Outline each Plasmodium falciparum-infected red blood cell.
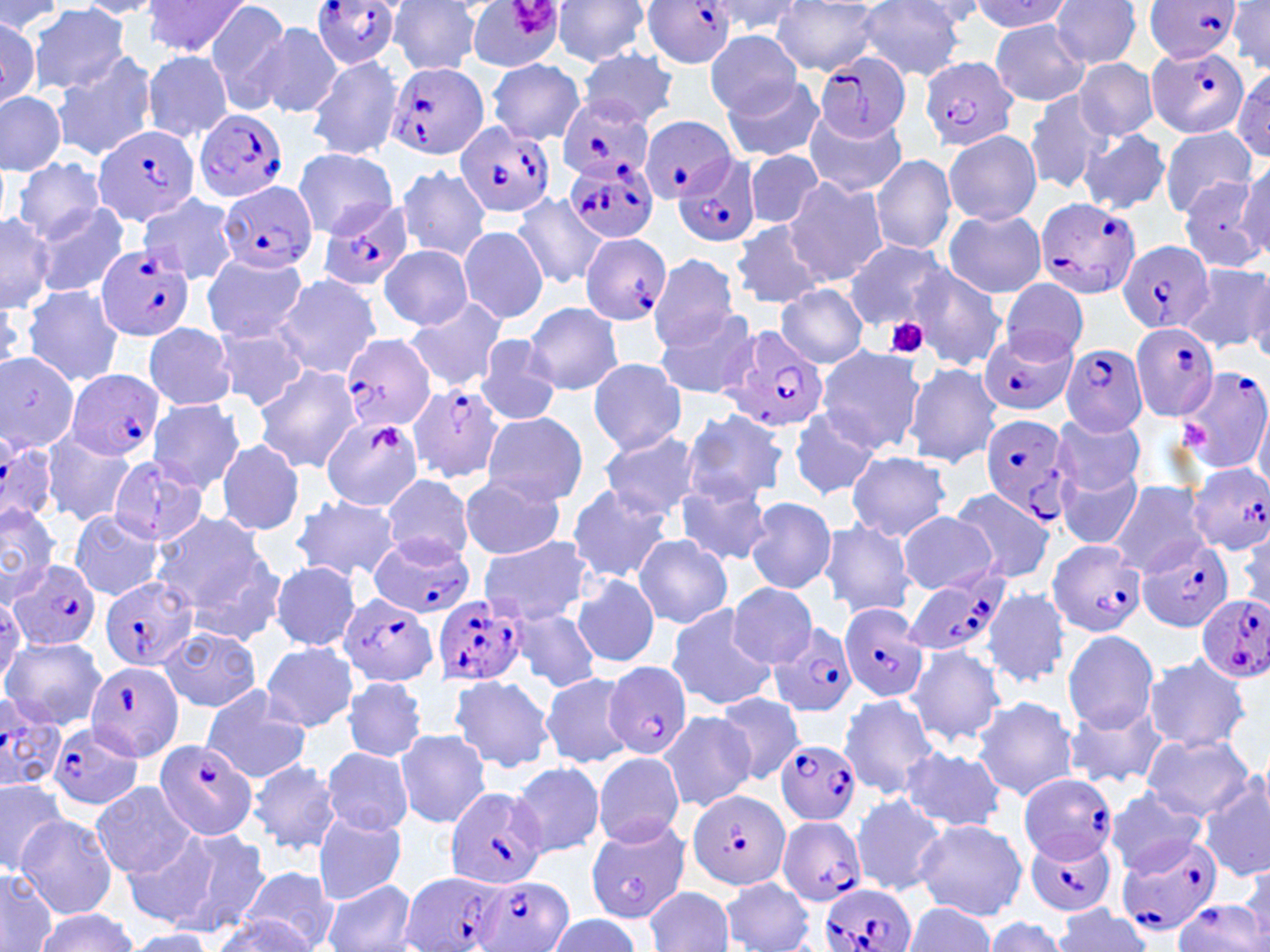
Approximate bounding boxes as [x1, y1, x2, y2] in pixels.
Plasmodium falciparum-infected red blood cells (subset): [309, 0, 402, 67], [641, 0, 737, 69], [1146, 1, 1240, 60], [1148, 42, 1250, 139], [816, 50, 912, 144], [920, 56, 1020, 151], [384, 62, 489, 161], [558, 96, 657, 183], [196, 108, 290, 204], [641, 117, 736, 202], [454, 121, 557, 219], [92, 123, 201, 226], [672, 155, 760, 245], [565, 156, 658, 245], [216, 181, 316, 275], [317, 197, 415, 292], [1032, 197, 1143, 302], [578, 233, 672, 326], [1118, 242, 1213, 334], [97, 243, 197, 342], [1130, 321, 1221, 423], [720, 326, 830, 432], [979, 327, 1077, 417], [340, 334, 436, 434], [1060, 343, 1149, 437], [1178, 367, 1270, 477], [68, 370, 164, 462], [401, 379, 508, 480], [978, 413, 1077, 526], [0, 441, 60, 525], [1185, 463, 1270, 555], [368, 533, 475, 619], [1135, 535, 1233, 631], [1045, 537, 1145, 637], [8, 558, 103, 653], [101, 575, 199, 673], [339, 592, 440, 689], [432, 595, 531, 685], [1196, 595, 1270, 682], [837, 603, 929, 704], [768, 621, 860, 719], [602, 660, 691, 762], [86, 662, 185, 761], [0, 696, 63, 794], [44, 721, 143, 812], [152, 738, 259, 840], [774, 739, 863, 827], [1018, 773, 1117, 865], [444, 786, 550, 888], [687, 790, 792, 891], [777, 816, 868, 907], [1025, 829, 1116, 918], [1115, 834, 1222, 936], [401, 871, 510, 952], [475, 875, 571, 952], [817, 884, 915, 952], [1173, 898, 1265, 952].

Summary:
  - Uninfected red blood cell locations (subset): [142, 0, 251, 59], [464, 0, 566, 71], [551, 0, 653, 67], [706, 0, 801, 37], [970, 0, 1073, 31], [1229, 0, 1270, 77], [72, 1, 165, 18], [204, 1, 290, 109], [389, 1, 487, 76], [772, 1, 882, 74], [856, 1, 967, 79], [1049, 1, 1142, 69], [0, 2, 67, 35], [28, 5, 131, 93], [250, 20, 343, 120], [989, 20, 1088, 107], [705, 30, 803, 116], [580, 49, 678, 125], [51, 50, 157, 161], [141, 51, 232, 142], [307, 55, 404, 160], [1074, 58, 1158, 140], [488, 59, 585, 144], [1233, 66, 1269, 158], [720, 74, 824, 162], [0, 90, 66, 174], [1023, 91, 1112, 193], [803, 108, 906, 198], [1159, 127, 1256, 218], [942, 129, 1042, 226], [1076, 130, 1170, 214], [290, 148, 399, 237], [743, 150, 824, 230], [869, 153, 957, 255], [12, 157, 107, 243], [395, 163, 490, 262], [1235, 164, 1269, 257], [784, 177, 888, 287], [1176, 177, 1268, 273], [511, 193, 606, 288], [139, 194, 238, 284], [28, 205, 129, 301], [942, 209, 1047, 299], [0, 213, 54, 313], [729, 219, 825, 309], [457, 225, 548, 325], [845, 239, 949, 332], [377, 246, 475, 328], [201, 252, 309, 343], [647, 252, 739, 353], [1178, 262, 1270, 355], [909, 265, 1007, 372], [272, 274, 382, 378], [1000, 281, 1088, 361], [20, 284, 126, 388], [777, 285, 868, 366], [402, 297, 510, 393], [524, 301, 625, 395], [653, 308, 761, 399], [143, 322, 235, 410], [212, 325, 311, 411], [475, 334, 563, 425], [816, 346, 925, 453], [0, 350, 82, 456], [588, 358, 687, 454], [903, 362, 1002, 467], [251, 365, 360, 472], [147, 398, 248, 493], [1254, 403, 1270, 493], [785, 407, 883, 501], [678, 408, 789, 507], [481, 411, 587, 506], [1052, 413, 1147, 495], [322, 416, 423, 512], [42, 432, 135, 526], [597, 433, 703, 518], [215, 438, 306, 537], [846, 450, 951, 542], [108, 457, 210, 547], [1058, 468, 1142, 548], [381, 475, 475, 564], [459, 475, 565, 559], [676, 479, 773, 565], [1108, 479, 1211, 575], [566, 483, 674, 581], [950, 490, 1056, 584], [290, 495, 400, 581], [745, 497, 837, 594], [0, 503, 58, 599], [150, 508, 278, 634], [70, 511, 164, 599], [898, 511, 996, 594], [818, 521, 915, 619], [633, 534, 733, 628], [479, 536, 594, 625], [269, 561, 361, 650], [573, 574, 659, 668], [727, 583, 818, 668], [983, 588, 1071, 687], [665, 604, 775, 711], [511, 606, 601, 691], [160, 627, 263, 711], [1062, 629, 1159, 733], [1, 637, 108, 730], [261, 642, 356, 730], [907, 646, 1008, 746], [1142, 654, 1251, 752], [539, 672, 636, 768], [448, 675, 553, 773], [343, 676, 426, 762], [199, 686, 313, 783], [714, 694, 806, 786], [839, 694, 941, 798], [972, 696, 1080, 802], [1061, 702, 1167, 788], [658, 711, 756, 812], [394, 728, 491, 828], [1141, 734, 1256, 820], [900, 745, 1006, 833], [322, 747, 413, 835], [591, 753, 685, 848], [246, 757, 343, 856], [511, 762, 604, 857], [1196, 770, 1270, 880], [0, 775, 70, 872], [89, 781, 200, 880], [1104, 787, 1208, 877], [851, 794, 950, 898], [312, 812, 408, 903], [15, 815, 119, 918], [584, 817, 691, 922], [914, 818, 1028, 920], [162, 824, 272, 937], [121, 829, 221, 929], [1242, 862, 1270, 947], [0, 866, 59, 952], [240, 866, 340, 950], [719, 877, 815, 952], [323, 878, 418, 952], [645, 886, 734, 952], [903, 902, 994, 952], [1052, 907, 1151, 952], [31, 910, 135, 952], [546, 914, 642, 951], [212, 915, 320, 952], [982, 917, 1069, 951], [123, 930, 216, 951]
  - Platelet locations: [509, 0, 553, 36], [884, 316, 929, 359], [1179, 420, 1210, 450], [370, 424, 401, 453]
  - Slide-level diagnosis: Plasmodium falciparum
  - Modality: light microscopy
  - Preparation: thin blood film
  - Magnification: 1000x
  - Field of view: single
  - Stain: May-Grünwald-Giemsa
  - Image size: 1270×952 pixels